Outline each Plasmodium falciparum-infected red blood cell.
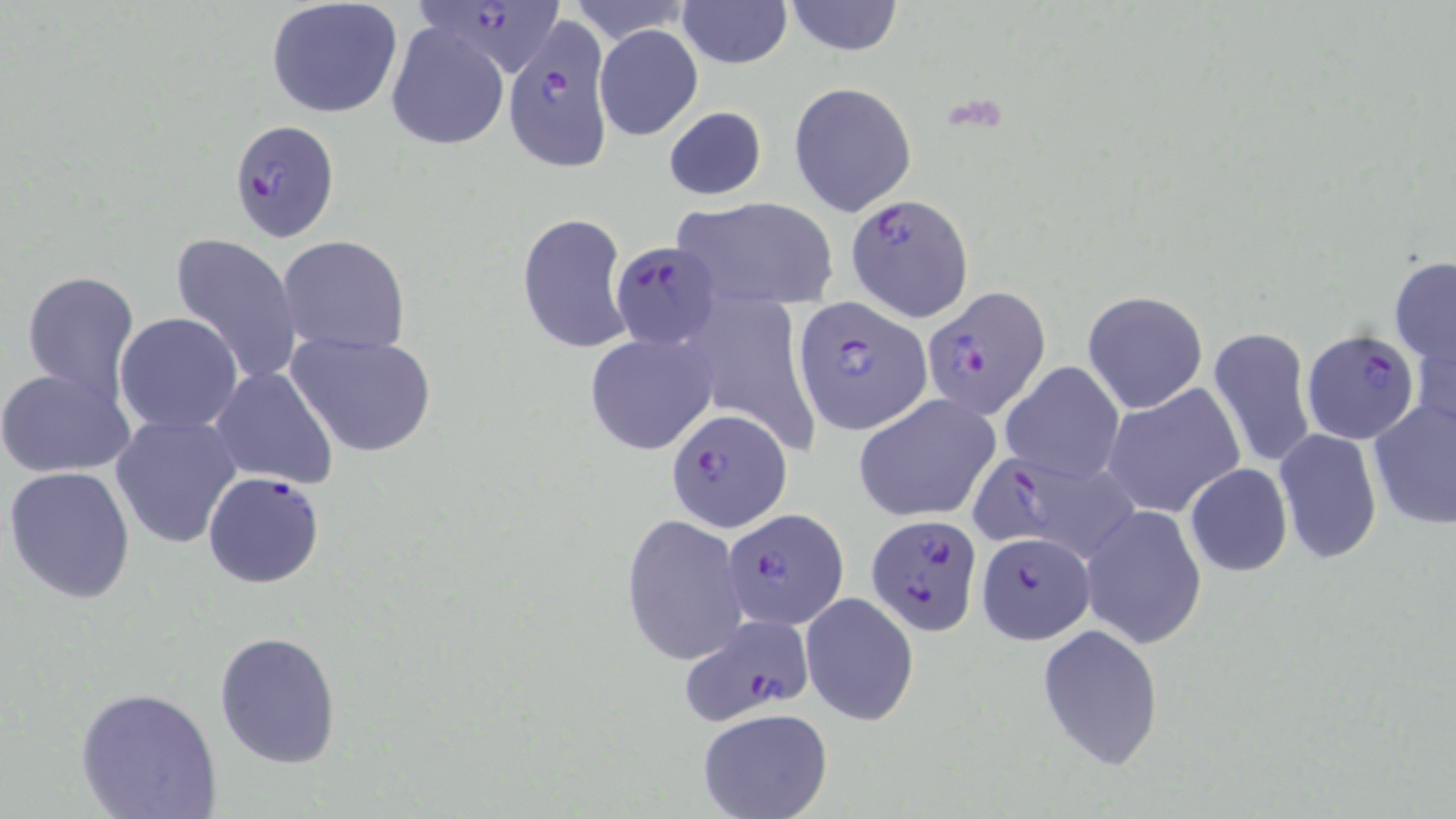

Approximate bounding boxes as [x1, y1, x2, y2] in pixels.
Plasmodium falciparum-infected red blood cells (subset): [420, 1, 570, 79], [232, 118, 344, 241], [845, 191, 974, 324], [611, 242, 724, 349], [922, 284, 1051, 421], [794, 297, 932, 435], [1301, 328, 1420, 445], [666, 410, 791, 534], [969, 454, 1140, 566], [723, 506, 851, 631], [865, 514, 983, 636], [975, 531, 1096, 643], [677, 614, 819, 724].

Summary:
  - Uninfected red blood cell locations (subset): [782, 0, 905, 57], [265, 1, 404, 120], [678, 1, 791, 69], [385, 21, 509, 151], [594, 24, 703, 140], [788, 81, 917, 218], [663, 106, 767, 200], [671, 197, 837, 310], [517, 212, 633, 354], [171, 232, 303, 384], [279, 236, 410, 354], [1388, 255, 1456, 369], [22, 269, 141, 401], [1083, 290, 1208, 414], [700, 300, 827, 452], [115, 312, 242, 435], [1411, 325, 1456, 443], [1207, 326, 1317, 471], [285, 332, 438, 458], [584, 332, 717, 456], [1001, 362, 1124, 484], [0, 367, 136, 478], [212, 368, 339, 490], [1102, 383, 1245, 519], [854, 394, 1000, 522], [1367, 397, 1456, 530], [111, 412, 242, 548], [1273, 429, 1382, 564], [1184, 463, 1293, 576], [4, 464, 136, 603], [203, 470, 327, 589], [1080, 505, 1207, 649], [621, 513, 748, 667], [799, 592, 920, 726], [1036, 624, 1164, 771], [213, 630, 342, 768], [75, 685, 222, 819], [696, 708, 834, 819]
  - Slide-level diagnosis: Plasmodium falciparum
  - Magnification: 1000x
  - Stain: May-Grünwald-Giemsa
  - Image size: 1456×819 pixels
  - Modality: optical microscopy
  - Preparation: thin blood smear
  - Field of view: single